Report the malaria status of this cell.
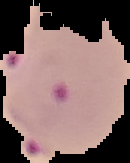

Parasitized.

The area outside the segmented cell region is set to black. From a thin blood film. Image is 130×163 pixels.